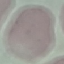

Malaria status: uninfected. Giemsa stain. Cell patch, automatically extracted from a larger field of view and resized to 64 × 64 pixels. Thin blood film. Acquired by smartphone through the microscope eyepiece.